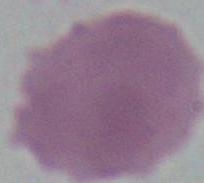
Summary:
  - Modality: photomicrograph
  - Identification: red blood cell
  - Magnification: 1000x